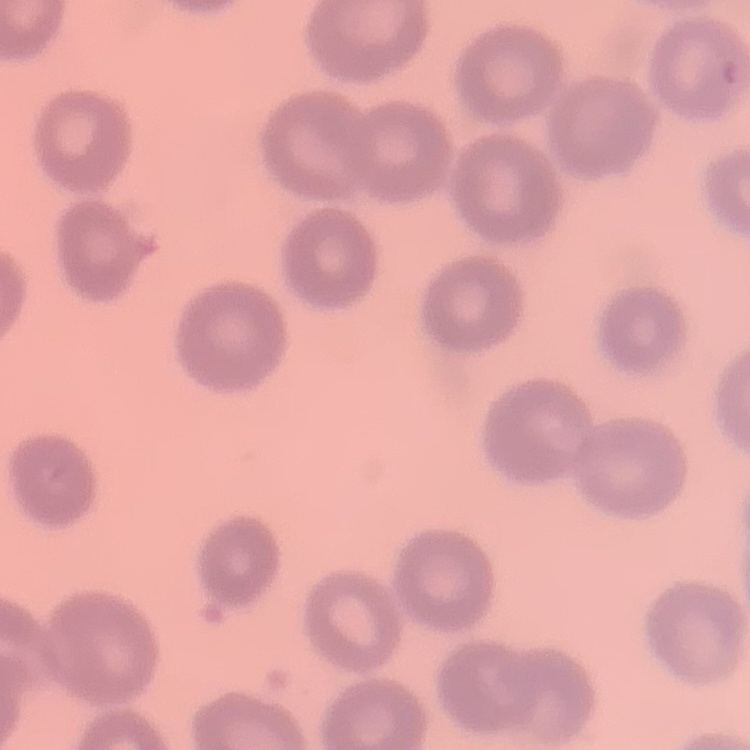 The erythrocytes show no rouleaux formation. One tile cut from a larger photomicrograph. Thin peripheral smear. Stained with either Field's or Giemsa.